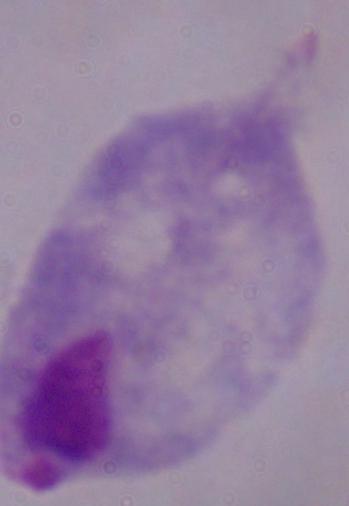

identification = trichomonad
magnification = 1000x
modality = micrograph